State which cell type is depicted.
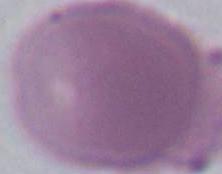
An erythrocyte.

Summary:
  - Modality: micrograph
  - Magnification: 1000x